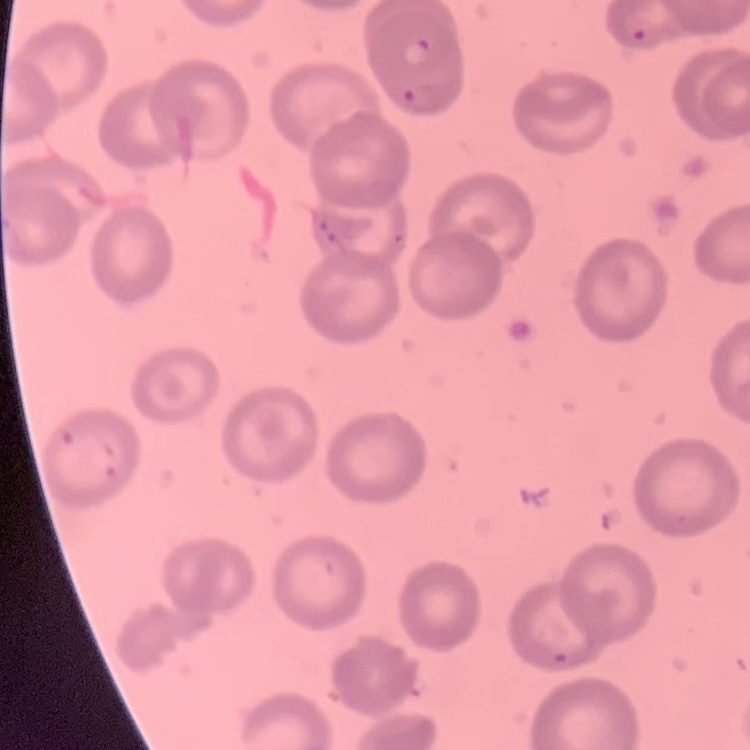
red blood cell morphology = no rouleaux formation
image type = square crop of a larger photomicrograph
preparation = thin blood film
stain = Field's or Giemsa